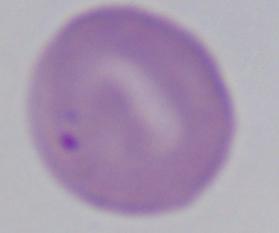 Captured at 1000x magnification. A Babesia parasite is shown. Photomicrograph.